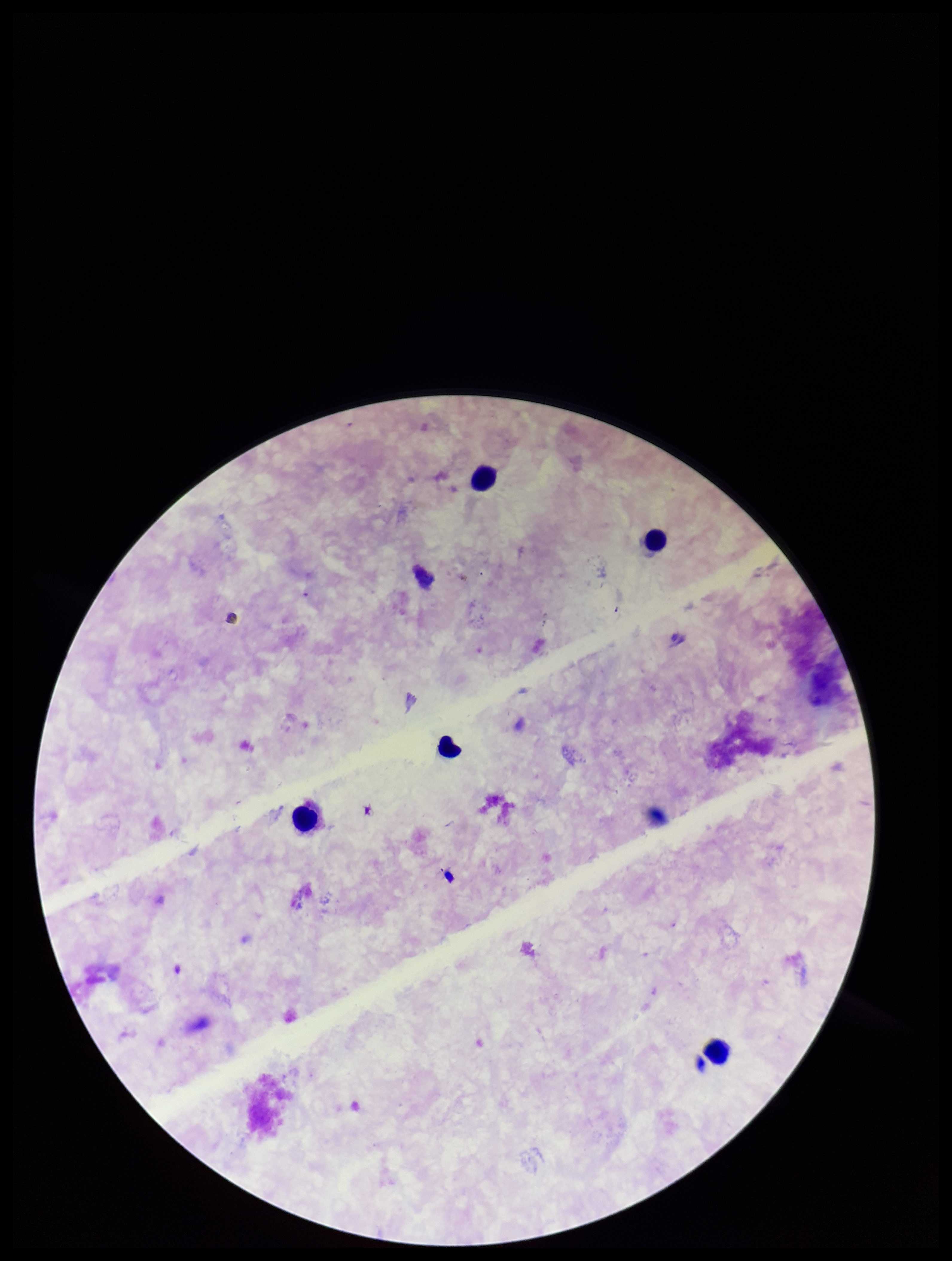
Summary:
  - Stain: Giemsa
  - Patient malaria status: negative
  - Preparation: thick blood smear
  - Parasite count: 0
  - Image size: 952×1261 pixels
  - Capture: smartphone photograph through the microscope eyepiece
  - Leukocyte count: 5
  - Field of view: single
  - Plasmodium parasites: none seen